Name the parasite shown.
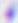

Toxoplasma gondii.

modality: photomicrograph
magnification: 400x